Report the malaria status of this cell.
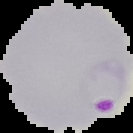

It is parasitized.

image_type: cell region segmented out of the field of view; surrounding area masked to black
preparation: thin blood smear
image_size: 133×133 pixels